Describe the morphology of the erythrocytes.
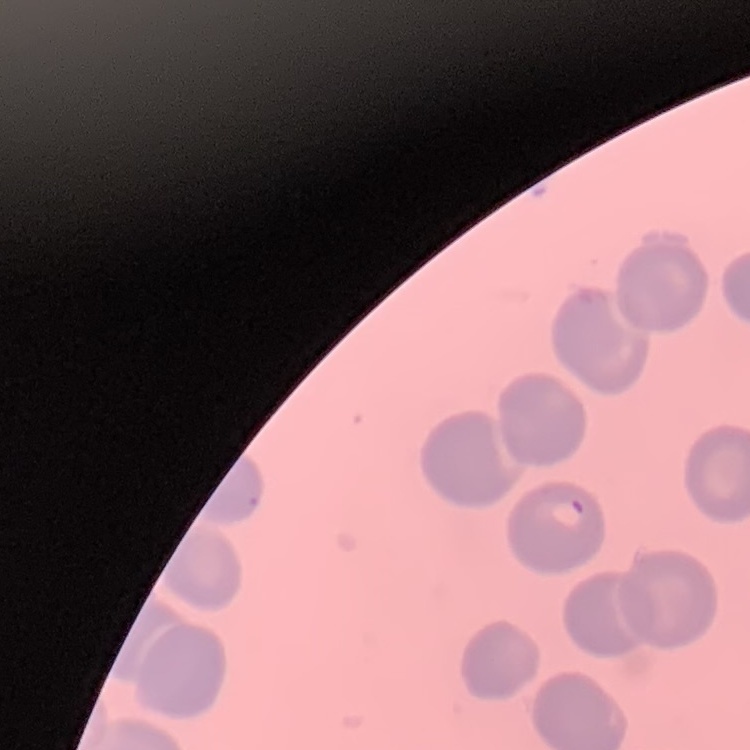
No rouleaux formation.

image type = square crop of a larger photomicrograph
stain = Field's or Giemsa
preparation = thin blood smear